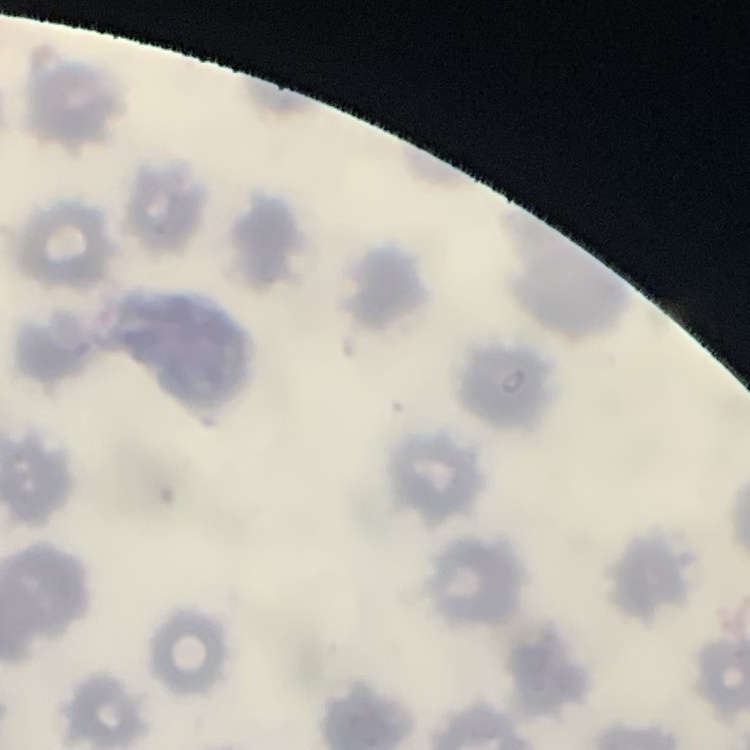
Summary:
  - Erythrocyte morphology: no rouleaux formation
  - Preparation: thin blood smear
  - Image type: square crop of a larger photomicrograph
  - Stain: Field's or Giemsa